State the blood parasite species.
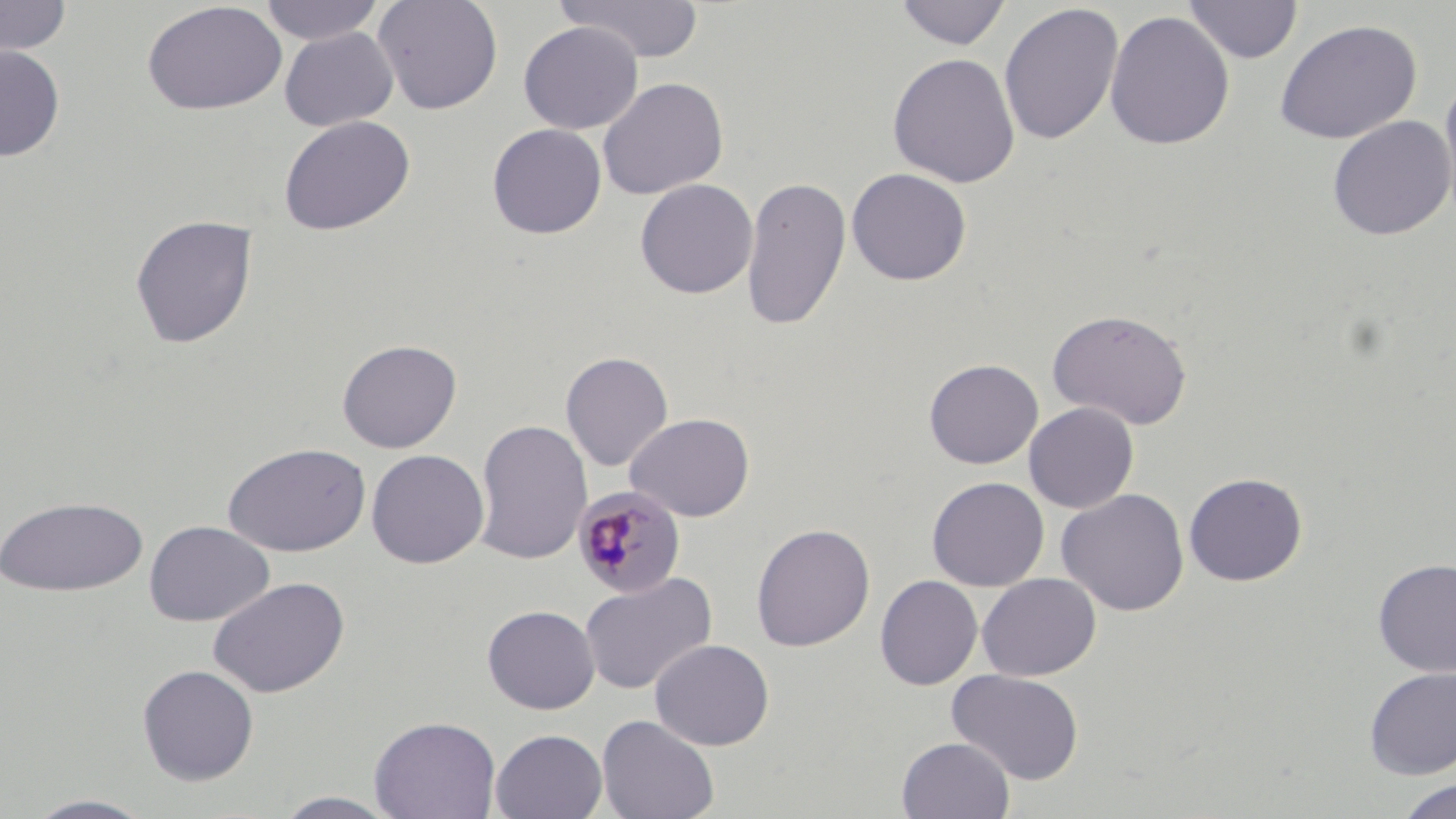
Plasmodium malariae.

{
  "uninfected_red_blood_cell_locations": "approximate bounding boxes as [x1, y1, x2, y2] in pixels: [0, 0, 72, 57], [259, 0, 386, 45], [373, 0, 504, 115], [554, 0, 705, 64], [893, 0, 1012, 50], [1183, 0, 1302, 63], [142, 2, 287, 115], [998, 3, 1124, 146], [1104, 10, 1235, 150], [1273, 19, 1422, 145], [518, 21, 643, 134], [279, 27, 399, 131], [0, 44, 65, 161], [887, 52, 1021, 188], [1438, 73, 1456, 228], [597, 76, 729, 200], [278, 115, 416, 236], [1327, 116, 1456, 240], [487, 123, 607, 239], [846, 167, 972, 286], [741, 174, 851, 331], [635, 178, 758, 299], [130, 214, 258, 349], [1047, 308, 1193, 430], [337, 338, 462, 453], [560, 351, 673, 472], [923, 358, 1043, 469], [1023, 402, 1139, 513], [625, 413, 754, 522], [473, 418, 593, 566], [222, 443, 370, 557], [366, 449, 489, 569], [1183, 472, 1308, 587], [926, 476, 1049, 591], [1056, 488, 1189, 616], [0, 495, 149, 597], [144, 520, 274, 626], [751, 522, 875, 652], [1373, 557, 1456, 676], [579, 571, 717, 695], [977, 573, 1101, 681], [875, 575, 983, 690], [208, 576, 349, 698], [481, 604, 600, 715], [649, 638, 774, 750], [136, 663, 259, 785], [1363, 667, 1456, 779], [947, 669, 1084, 785], [597, 714, 720, 819], [369, 715, 501, 819], [490, 728, 608, 819], [897, 736, 1015, 819], [1395, 778, 1456, 818], [272, 791, 405, 818], [22, 794, 159, 818]",
  "plasmodium_malariae_infected_red_blood_cell_locations": "approximate bounding boxes as [x1, y1, x2, y2] in pixels: [572, 485, 687, 599]",
  "image_size": "1456×819 pixels",
  "magnification": "1000x",
  "field_of_view": "single",
  "modality": "light microscopy",
  "stain": "May-Grünwald-Giemsa",
  "preparation": "thin blood smear"
}